Report the malaria status of this cell.
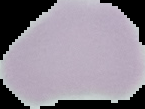

It is uninfected.

Summary:
  - Preparation: thin blood film
  - Image size: 145×109 pixels
  - Image type: segmented cell region with the area outside set to black